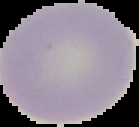
Summary:
  - Result: negative for Plasmodium parasites
  - Image type: cell region segmented out of the field of view; surrounding area masked to black
  - Preparation: thin blood film
  - Image size: 139×127 pixels